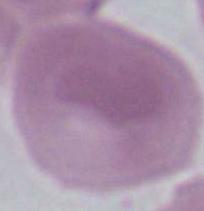
Summary:
  - Magnification: 1000x
  - Modality: micrograph
  - Identification: erythrocyte